Locate every blood parasite and identify its species.
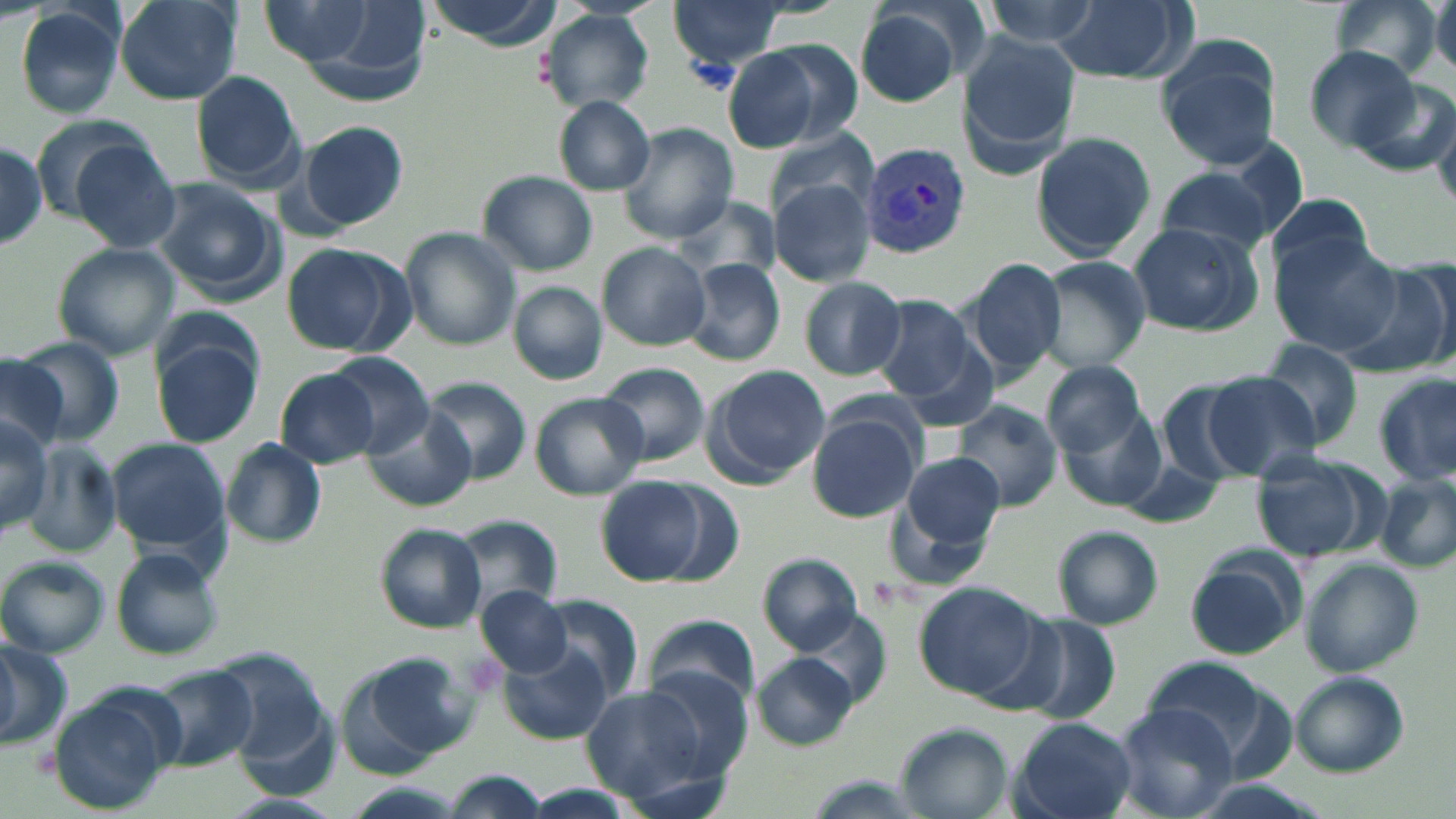
Approximate bounding boxes as (x1,y1)-(x2,y2) corner pairs in pixels.
Plasmodium vivax-infected red blood cells: (859,141)-(969,260).
No Plasmodium falciparum, Plasmodium ovale, Plasmodium malariae, Babesia divergens, or Trypanosoma brucei observed.

Uninfected red blood cell locations: (116,0)-(244,106), (424,0)-(559,46), (1050,0)-(1193,83), (1328,0)-(1448,79), (979,1)-(1100,48), (670,2)-(785,68), (1432,2)-(1454,75), (264,4)-(371,63), (850,4)-(975,107), (9,6)-(128,122), (541,9)-(656,115), (956,34)-(1081,168), (1156,37)-(1280,169), (722,42)-(849,154), (1306,45)-(1427,152), (191,70)-(306,190), (1350,74)-(1455,180), (1429,93)-(1456,213), (555,97)-(655,194), (29,116)-(157,221), (299,121)-(406,228), (618,122)-(737,245), (768,129)-(878,223), (1029,131)-(1156,261), (0,136)-(47,251), (72,143)-(182,252), (1156,167)-(1275,257), (479,171)-(597,275), (153,179)-(282,298), (772,181)-(877,286), (1265,192)-(1378,286), (680,194)-(778,285), (1128,222)-(1263,335), (401,227)-(521,351), (1271,234)-(1404,354), (596,242)-(712,349), (51,243)-(179,360), (280,243)-(411,356), (966,256)-(1068,380), (1033,256)-(1153,372), (685,258)-(786,366), (1340,262)-(1456,376), (800,277)-(906,379), (508,281)-(608,384), (871,296)-(975,402), (887,318)-(1001,431), (11,336)-(123,447), (152,337)-(262,448), (1256,339)-(1366,450), (327,353)-(434,453), (0,355)-(66,449), (1042,360)-(1146,453), (600,363)-(710,465), (705,364)-(830,482), (277,369)-(378,467), (1203,372)-(1322,479), (1373,373)-(1455,485), (422,376)-(532,484), (1156,381)-(1255,483), (527,392)-(648,500), (954,401)-(1062,511), (364,406)-(476,512), (1061,406)-(1167,513), (807,409)-(923,522), (0,413)-(51,532), (110,439)-(227,555), (220,439)-(327,548), (25,443)-(123,555), (896,449)-(1008,552), (1250,453)-(1379,563), (1376,476)-(1456,574), (595,477)-(706,585), (450,514)-(565,615), (374,523)-(484,633), (1052,525)-(1164,630), (110,548)-(224,663), (759,552)-(864,653), (1183,552)-(1304,661), (0,557)-(109,657), (1300,560)-(1422,675), (916,584)-(1042,701), (476,586)-(575,677), (529,594)-(641,693), (804,609)-(890,709), (644,614)-(758,712), (1018,616)-(1122,726), (0,636)-(71,749), (504,646)-(610,744), (753,652)-(860,749), (347,653)-(474,770), (220,657)-(334,783), (1140,657)-(1287,769), (145,665)-(258,770), (644,668)-(754,782), (1289,670)-(1408,777), (581,684)-(716,806), (47,691)-(179,814), (1112,703)-(1239,819), (1012,718)-(1137,819), (894,723)-(1011,819), (444,770)-(550,818). Slide-level diagnosis: Plasmodium vivax. May-Grünwald-Giemsa stain. Optical microscopy. Captured at 1000x magnification. Image is 1456×819 pixels. Thin blood smear. One field of a larger specimen.